Locate every blood parasite and identify its species.
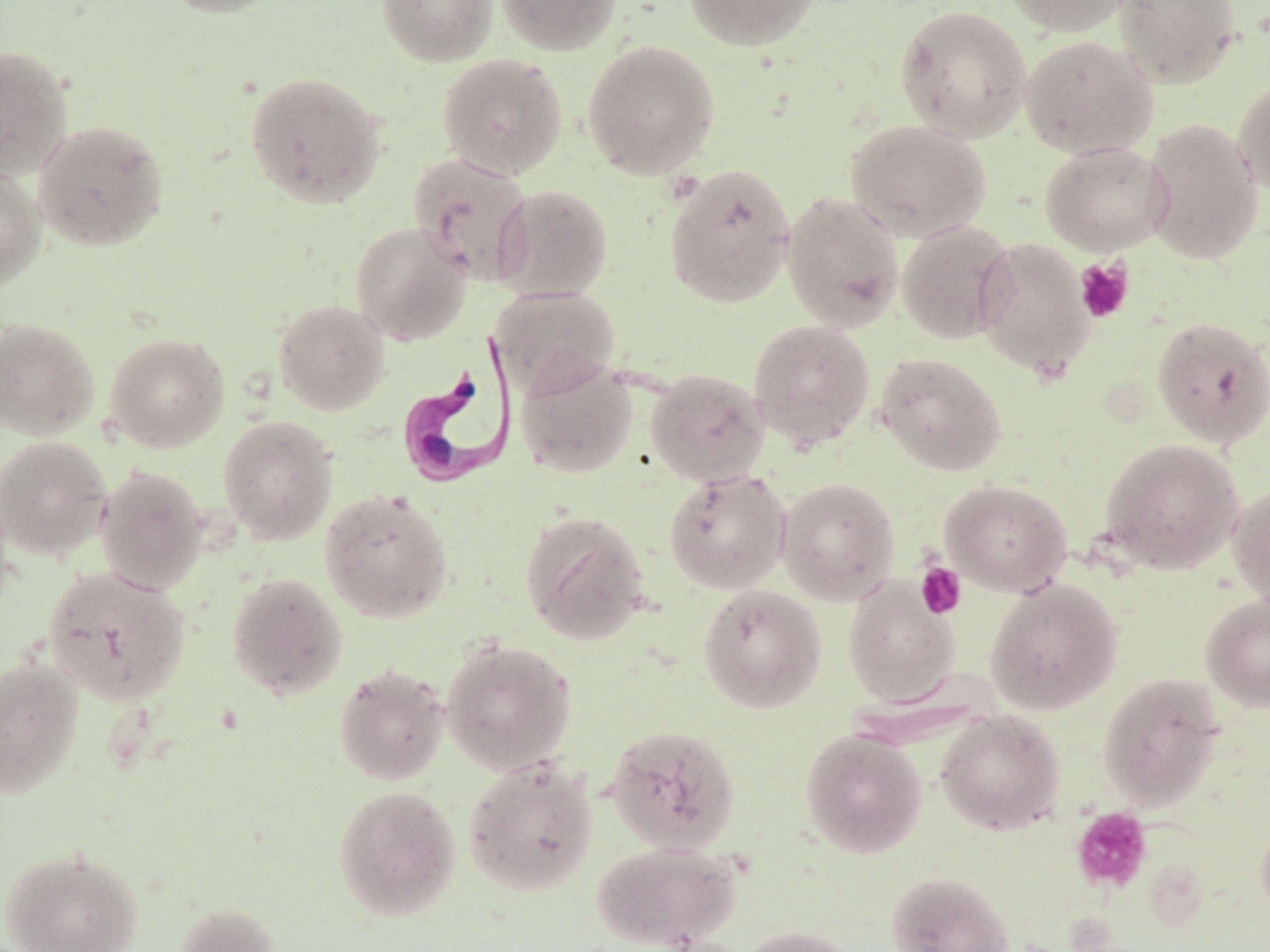
Approximate bounding boxes as [x1, y1, x2, y2] in pixels.
Trypanosoma brucei: [396, 331, 520, 492].
No Plasmodium falciparum, Plasmodium ovale, Plasmodium malariae, Plasmodium vivax, or Babesia divergens observed.

{
  "slide_level_diagnosis": "Trypanosoma brucei",
  "modality": "optical microscopy",
  "image_size": "1270×952 pixels",
  "stain": "May-Grünwald-Giemsa",
  "platelet_locations": "approximate bounding boxes as [x1, y1, x2, y2] in pixels: [1074, 257, 1135, 324], [915, 562, 967, 618], [1070, 806, 1153, 893]",
  "uninfected_red_blood_cell_locations": "approximate bounding boxes as [x1, y1, x2, y2] in pixels: [160, 0, 286, 18], [375, 0, 497, 66], [494, 0, 621, 55], [684, 0, 819, 51], [1001, 0, 1138, 36], [1113, 0, 1241, 89], [893, 4, 1033, 142], [1019, 34, 1157, 158], [582, 40, 720, 180], [0, 44, 74, 179], [437, 53, 568, 179], [244, 70, 388, 209], [1233, 75, 1270, 199], [1142, 117, 1263, 265], [31, 119, 170, 252], [845, 119, 992, 242], [1039, 141, 1172, 256], [408, 152, 535, 284], [0, 163, 47, 291], [664, 163, 796, 309], [493, 185, 613, 301], [781, 190, 905, 333], [896, 219, 1017, 345], [349, 221, 472, 346], [974, 236, 1095, 380], [489, 286, 620, 396], [273, 298, 391, 415], [0, 316, 99, 441], [1151, 316, 1270, 448], [747, 319, 876, 452], [104, 332, 229, 453], [874, 352, 1007, 477], [515, 356, 638, 478], [645, 368, 770, 487], [217, 414, 338, 545], [0, 435, 112, 562], [1098, 439, 1244, 574], [95, 465, 209, 595], [663, 468, 791, 594], [776, 477, 900, 605], [939, 479, 1072, 596], [1226, 482, 1270, 609], [319, 487, 454, 624], [519, 509, 651, 645], [41, 566, 191, 706], [226, 572, 348, 700], [842, 575, 960, 707], [984, 579, 1123, 715], [697, 582, 827, 714], [1200, 593, 1270, 713], [440, 638, 578, 775], [0, 655, 84, 799], [333, 663, 450, 786], [1098, 672, 1226, 810], [935, 709, 1065, 835], [604, 723, 741, 854], [799, 727, 927, 858], [463, 757, 599, 896], [333, 784, 461, 922], [1255, 815, 1270, 922], [589, 840, 741, 951], [1, 846, 143, 952], [885, 871, 1013, 952], [174, 903, 283, 952], [738, 924, 860, 952]",
  "field_of_view": "single",
  "magnification": "1000x",
  "preparation": "thin blood smear"
}